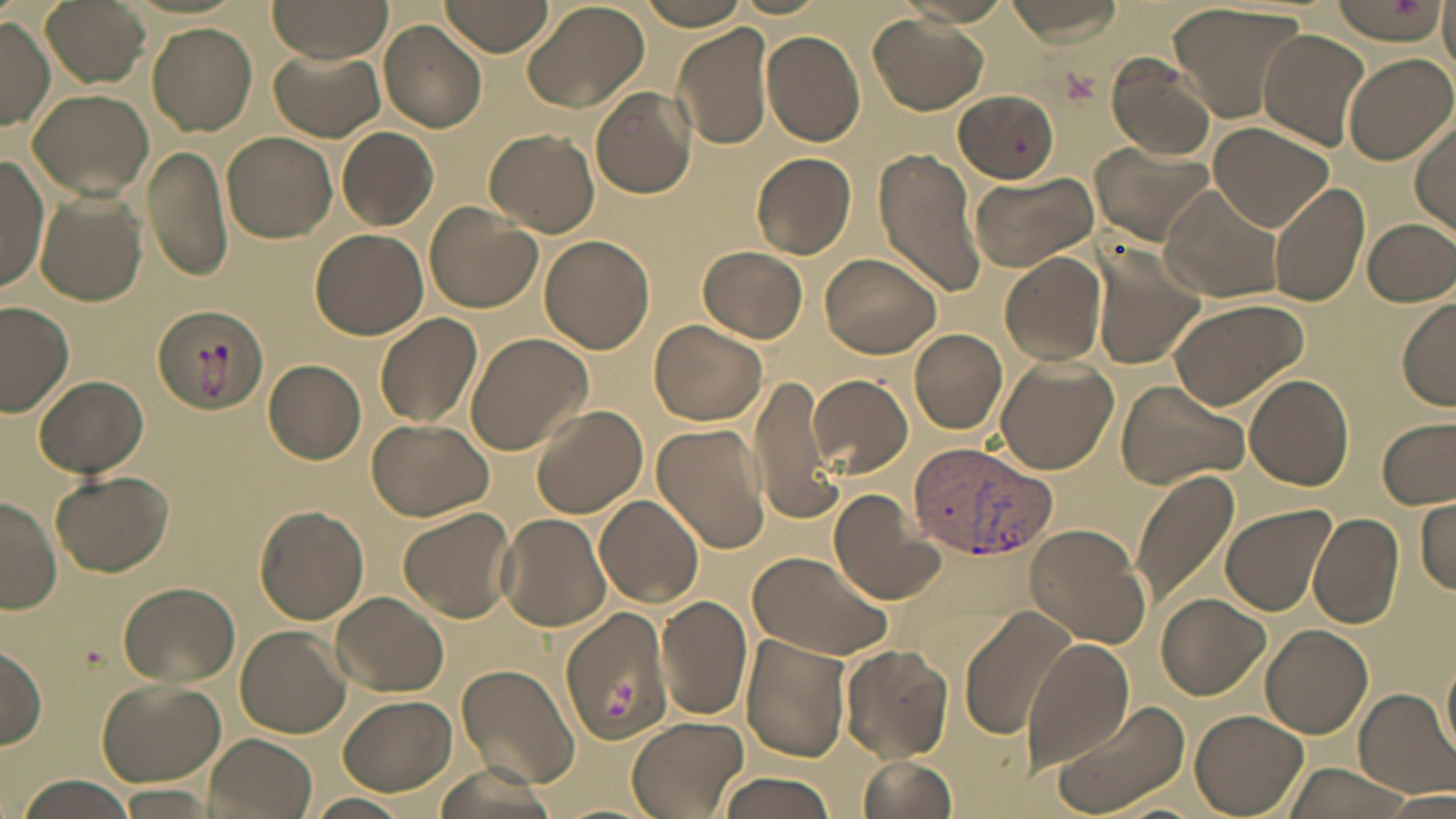
Summary:
  - Coordinate format: approximate bounding boxes as (x1, y1, x2, y2) in pixels
  - Plasmodium vivax-infected red blood cell locations: (906, 442, 1057, 560)
  - Platelet locations: (1011, 135, 1030, 156), (601, 677, 635, 721)
  - Uninfected red blood cell locations: (267, 0, 394, 61), (442, 0, 554, 56), (519, 0, 650, 114), (636, 0, 752, 30), (894, 0, 1014, 29), (1007, 0, 1126, 46), (41, 1, 149, 89), (1326, 1, 1444, 44), (1166, 3, 1311, 123), (868, 13, 988, 115), (0, 17, 53, 130), (379, 19, 487, 132), (148, 23, 257, 136), (672, 23, 775, 151), (762, 29, 866, 148), (1258, 30, 1371, 152), (269, 48, 385, 142), (1341, 52, 1454, 166), (1104, 53, 1215, 163), (591, 86, 697, 199), (952, 88, 1059, 180), (28, 90, 154, 200), (1412, 118, 1456, 234), (1208, 122, 1334, 232), (337, 127, 437, 229), (485, 128, 598, 237), (223, 132, 337, 243), (1087, 140, 1216, 247), (144, 143, 234, 282), (872, 149, 986, 298), (751, 152, 857, 258), (0, 157, 49, 292), (966, 172, 1098, 272), (1266, 179, 1371, 307), (1157, 185, 1288, 304), (35, 191, 147, 304), (423, 202, 542, 314), (1362, 217, 1455, 307), (310, 229, 428, 340), (539, 235, 654, 355), (1087, 242, 1207, 369), (697, 246, 809, 343), (1000, 249, 1111, 366), (818, 252, 942, 359), (1397, 295, 1456, 409), (1164, 297, 1310, 409), (0, 302, 75, 418), (149, 304, 266, 423), (375, 314, 482, 429), (650, 320, 768, 427), (910, 328, 1007, 433), (465, 333, 592, 455), (993, 357, 1117, 473), (263, 358, 366, 464), (809, 375, 912, 476), (1243, 375, 1354, 491), (36, 376, 147, 476), (746, 377, 843, 524), (1115, 378, 1250, 490), (530, 405, 647, 517), (365, 417, 496, 522), (1377, 418, 1454, 509), (650, 422, 771, 555), (1130, 466, 1241, 609), (49, 470, 172, 577), (825, 488, 945, 606), (0, 493, 60, 615), (594, 493, 704, 609), (1415, 497, 1455, 596), (255, 505, 370, 624), (1220, 505, 1336, 616), (397, 506, 518, 623), (1307, 510, 1404, 628), (497, 511, 614, 632), (1023, 523, 1151, 647), (747, 550, 890, 661), (118, 581, 240, 687), (333, 592, 448, 697), (656, 594, 752, 721), (1157, 594, 1268, 699), (959, 604, 1076, 740), (559, 605, 675, 744), (1262, 624, 1372, 737), (235, 626, 350, 737), (740, 633, 851, 763), (1022, 637, 1136, 771), (839, 642, 954, 763), (0, 643, 47, 747), (1441, 648, 1456, 763), (456, 663, 578, 791), (95, 678, 226, 786), (1353, 688, 1456, 797), (336, 693, 456, 795), (1046, 698, 1191, 817), (1189, 708, 1307, 815), (625, 716, 748, 818), (207, 733, 319, 819), (855, 752, 959, 819), (1277, 761, 1418, 819), (435, 764, 553, 819), (713, 771, 838, 818), (17, 774, 143, 817), (119, 784, 222, 814), (1381, 789, 1455, 815), (303, 793, 412, 819)
  - Slide-level diagnosis: Plasmodium vivax
  - Field of view: single
  - Preparation: thin blood film
  - Image size: 1456×819 pixels
  - Modality: optical microscopy
  - Magnification: 1000x
  - Stain: May-Grünwald-Giemsa